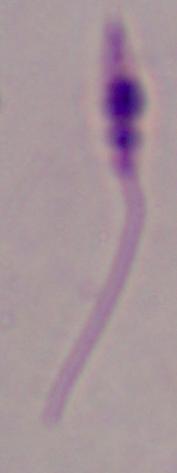 A Leishmania parasite is seen. 1000x magnification. Micrograph.